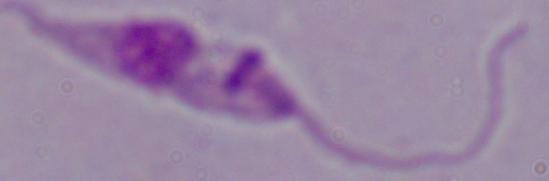
Summary:
  - Identification: Leishmania
  - Magnification: 1000x
  - Modality: photomicrograph